Name the parasite shown.
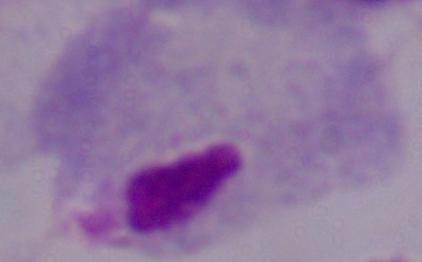
A trichomonad.

Summary:
  - Modality: micrograph
  - Magnification: 1000x